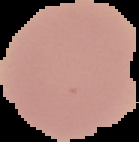

From a thin blood smear. Malaria status: uninfected. Image is 139×142 pixels. The area outside the segmented cell region is set to black.